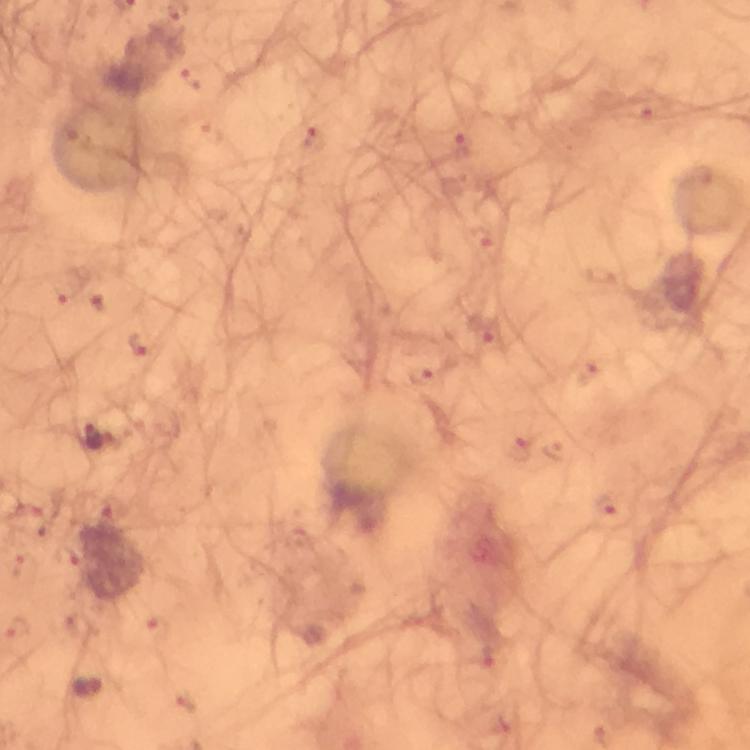

Approximate centers as (x, y) in pixels.
Summary:
  - Plasmodium parasite locations: (92, 434)
  - Image size: 750×750 pixels
  - Cropped from: one field of view
  - Immersion oil: used
  - Preparation: thick smear
  - Stain: Giemsa
  - Capture: smartphone camera through the microscope
  - Magnification: 100x
  - Context: from a diagnostic examination for malaria